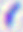

Captured at 400x magnification. Photomicrograph. Toxoplasma gondii is seen.